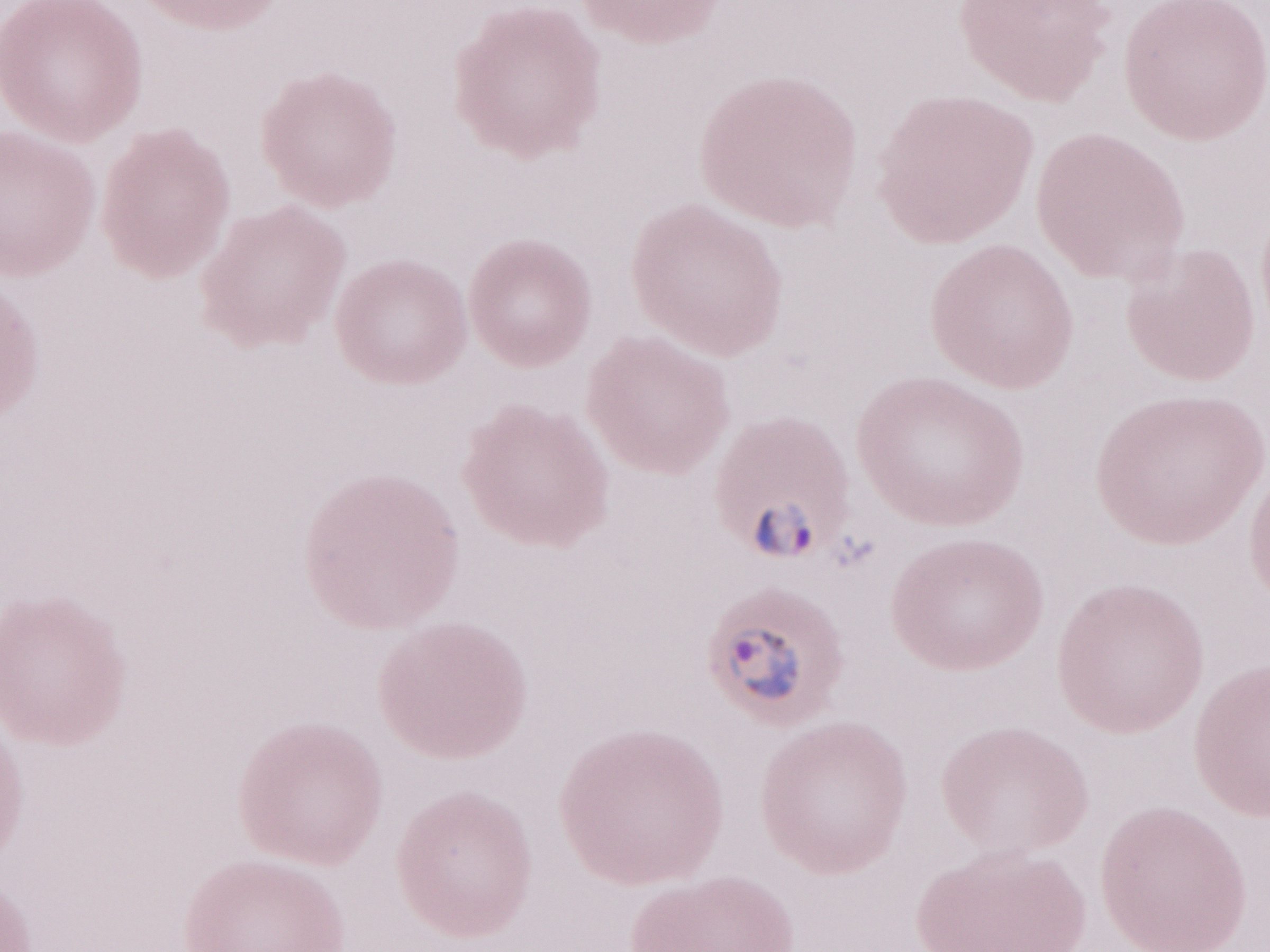

Thin peripheral-blood smear. Patient-level malaria diagnosis: positive. One field of this slide. May-Grünwald-Giemsa-stained preparation. Olympus BX43 microscope and DP73 digital camera. Magnification: 1,000x. Image is 1270×952 pixels.